Name the parasite shown.
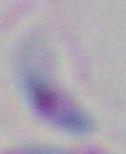
This is Toxoplasma gondii.

Summary:
  - Magnification: 1000x
  - Modality: micrograph